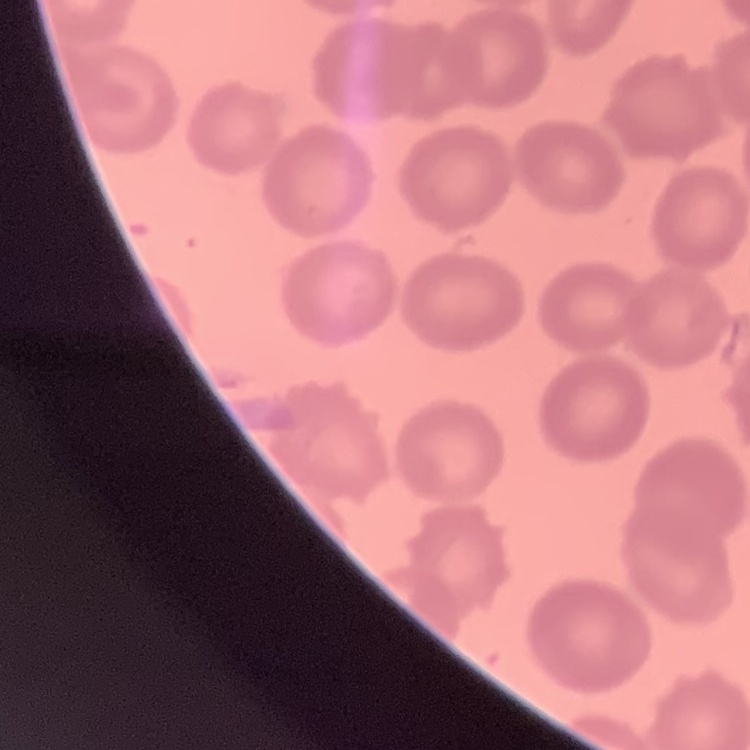

Summary:
  - Red blood cell morphology: no rouleaux formation
  - Preparation: thin blood smear
  - Stain: Field's or Giemsa
  - Image type: square crop of a larger photomicrograph